Name the cell type shown.
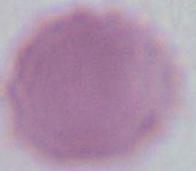
This is an erythrocyte.

modality = micrograph
magnification = 1000x